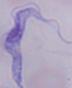
Summary:
  - Identification: trypanosome
  - Modality: photomicrograph
  - Magnification: 1000x